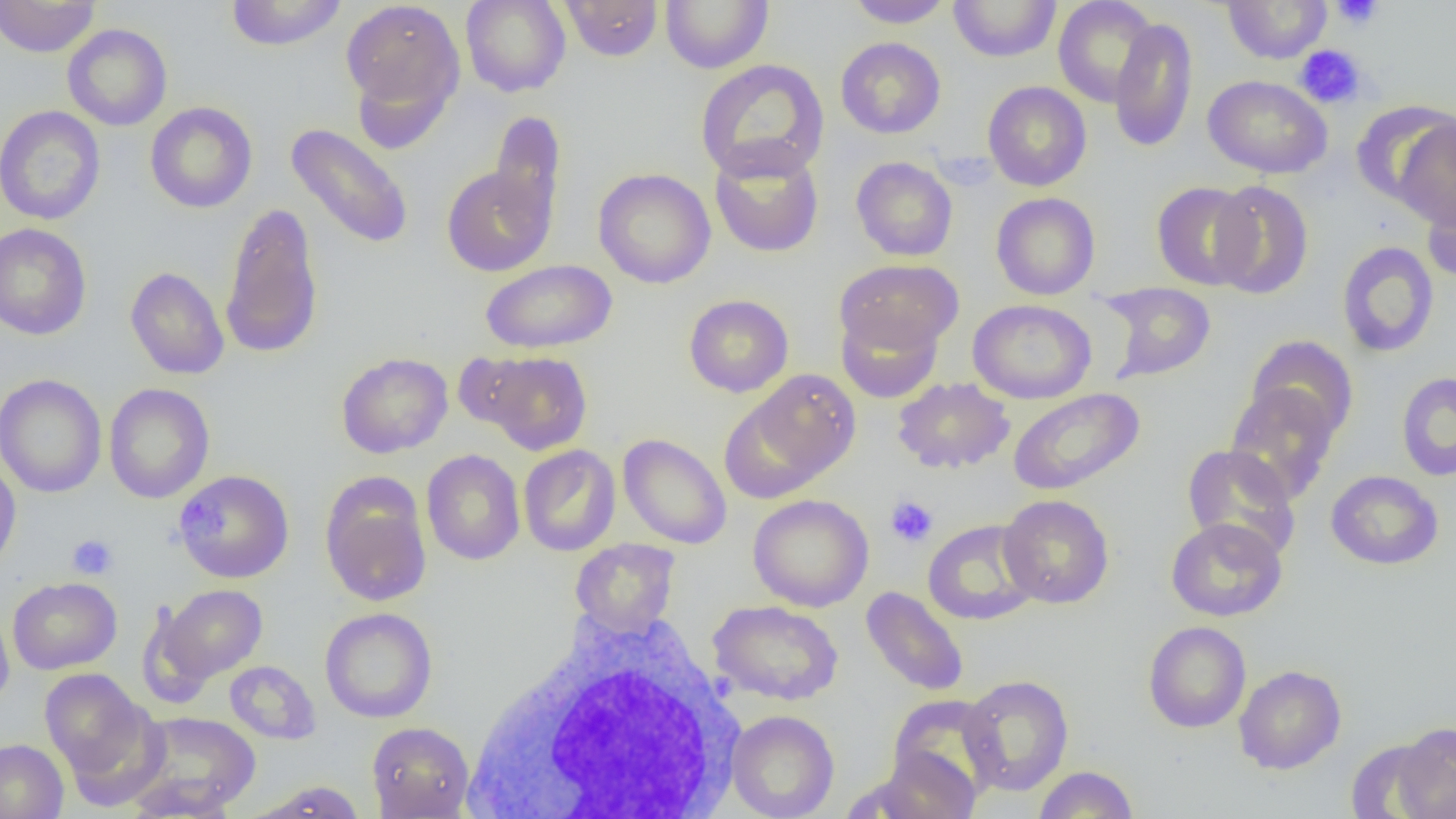

Approximate bounding boxes as [x1, y1, x2, y2] in pixels. White blood cell locations: [467, 607, 749, 815]. Platelet locations: [1330, 0, 1384, 30], [1294, 45, 1365, 109], [885, 495, 939, 548], [67, 534, 118, 579]. Uninfected red blood cell locations: [0, 0, 100, 57], [225, 0, 347, 51], [340, 0, 465, 126], [460, 0, 571, 97], [561, 0, 663, 61], [660, 0, 773, 74], [845, 0, 954, 28], [1053, 0, 1159, 108], [949, 1, 1062, 62], [1223, 1, 1332, 64], [1109, 17, 1198, 153], [62, 23, 173, 131], [835, 37, 946, 139], [695, 59, 830, 183], [1203, 75, 1332, 178], [982, 81, 1092, 191], [145, 101, 257, 213], [1351, 101, 1454, 208], [1, 105, 105, 225], [489, 110, 567, 237], [1394, 118, 1456, 229], [285, 123, 414, 250], [709, 142, 824, 257], [851, 157, 958, 261], [441, 165, 555, 276], [593, 167, 716, 289], [1209, 180, 1314, 299], [1151, 181, 1258, 290], [1421, 183, 1456, 285], [991, 192, 1101, 300], [219, 201, 325, 359], [0, 223, 92, 340], [1336, 241, 1440, 358], [480, 259, 617, 354], [835, 259, 962, 356], [125, 266, 229, 379], [1097, 281, 1217, 383], [683, 294, 794, 398], [968, 299, 1097, 404], [836, 308, 942, 403], [1246, 335, 1359, 443], [481, 351, 592, 454], [337, 352, 453, 458], [746, 369, 861, 482], [1395, 372, 1456, 481], [0, 373, 107, 498], [892, 377, 1015, 474], [103, 383, 215, 504], [1224, 383, 1340, 503], [1007, 388, 1144, 496], [719, 393, 835, 503], [617, 433, 732, 549], [1182, 444, 1302, 561], [518, 445, 620, 556], [422, 449, 525, 565], [0, 456, 21, 574], [174, 469, 294, 583], [1325, 470, 1444, 570], [320, 478, 433, 607], [748, 494, 874, 612], [998, 494, 1114, 609], [1166, 517, 1287, 621], [922, 520, 1040, 625], [570, 538, 680, 636], [7, 577, 122, 674], [160, 585, 267, 682], [861, 586, 969, 696], [708, 600, 844, 705], [135, 602, 218, 709], [0, 606, 14, 710], [320, 607, 437, 723], [1143, 621, 1251, 733], [224, 660, 320, 744], [1234, 664, 1346, 774], [40, 668, 150, 778], [959, 675, 1074, 796], [887, 695, 1002, 802], [726, 709, 839, 819], [129, 711, 262, 813], [366, 722, 474, 818], [1393, 722, 1456, 818], [0, 738, 68, 819], [1345, 738, 1446, 819], [865, 747, 980, 819], [1033, 765, 1139, 819], [124, 776, 239, 819], [248, 780, 367, 818]. Slide-level diagnosis: no evidence of blood parasites. Image is 1456×819 pixels. Captured at 1000x magnification. Thin blood film. Light microscopy. One field of a larger specimen.